Assess this cell for malaria.
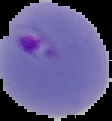

It is parasitized.

image type = segmented cell region on a black background
preparation = thin blood smear
image size = 112×121 pixels